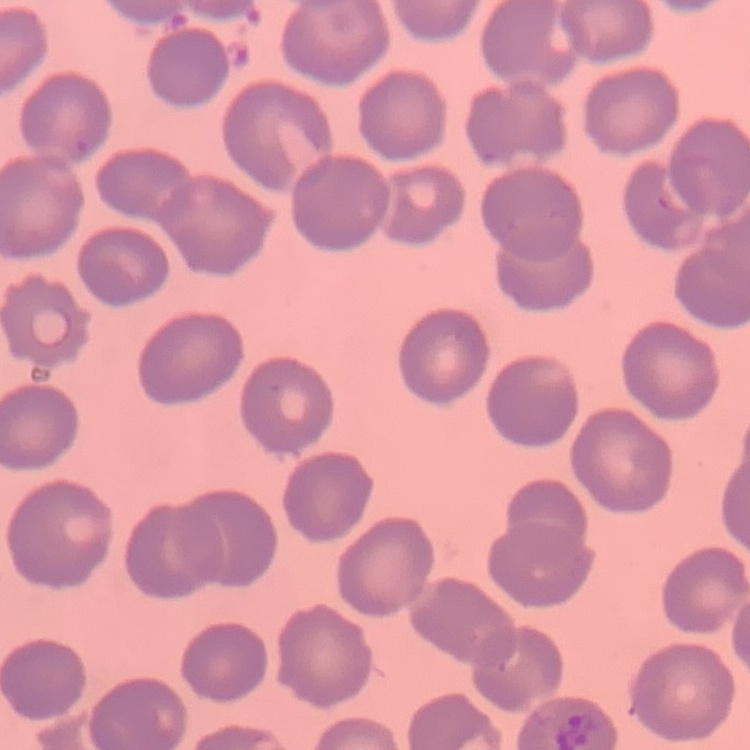

The erythrocytes exhibit no rouleaux formation. One tile cut from a larger photomicrograph. Stained with either Field's or Giemsa. Thin blood smear.